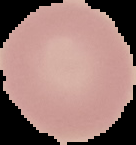

Summary:
  - Image size: 136×145 pixels
  - Preparation: thin blood smear
  - Image type: cell region segmented out of the field of view; surrounding area masked to black
  - Malaria status: uninfected